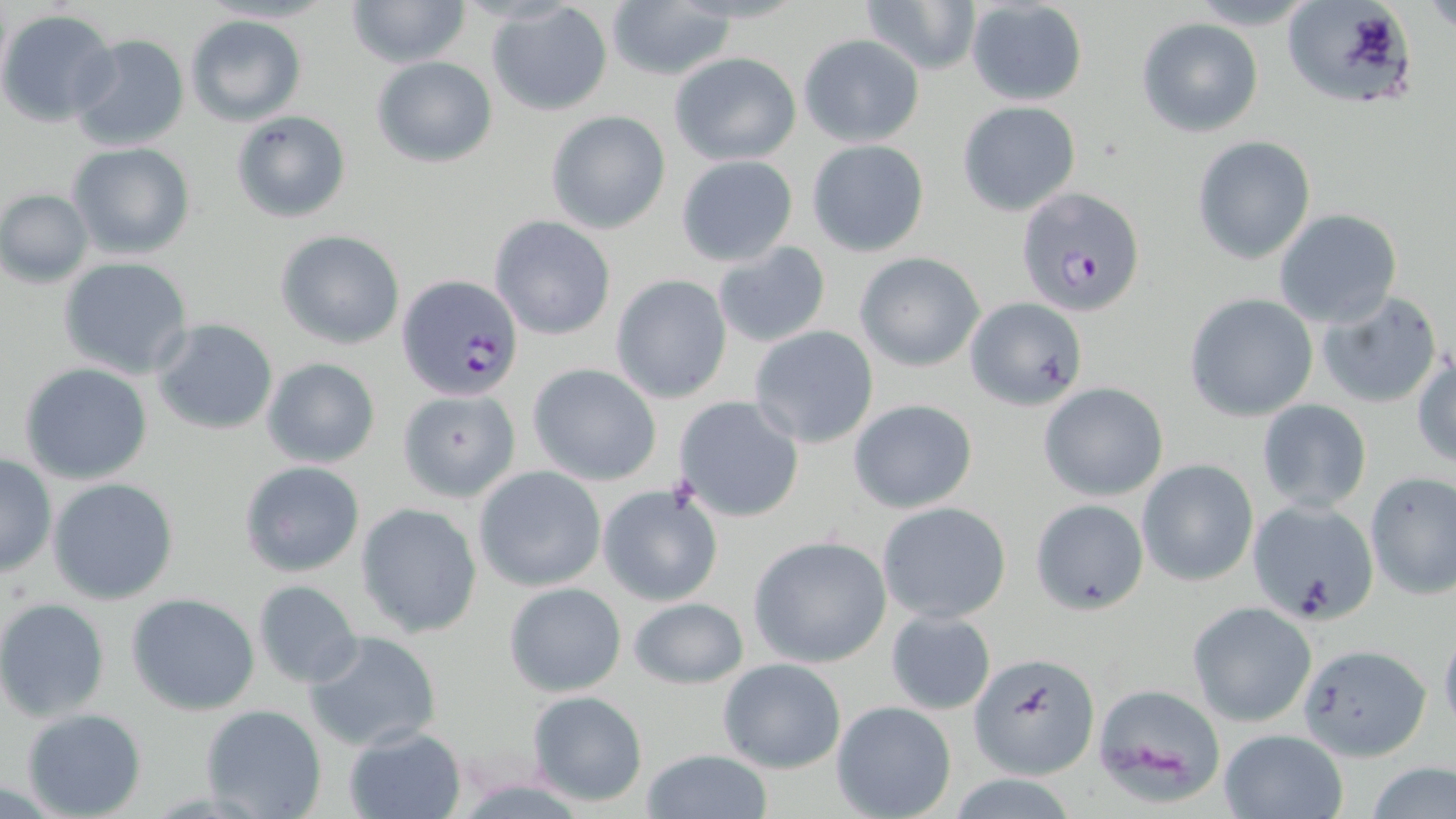

{
  "slide_level_diagnosis": "Plasmodium falciparum",
  "magnification": "1000x",
  "stain": "May-Grünwald-Giemsa",
  "field_of_view": "one of a larger specimen",
  "uninfected_red_blood_cell_locations": "approximate bounding boxes as (x1, y1, x2, y2) in pixels: (346, 0, 470, 68), (860, 0, 981, 77), (1282, 0, 1421, 111), (1424, 0, 1456, 34), (965, 1, 1089, 106), (605, 2, 733, 81), (487, 4, 614, 116), (0, 10, 119, 125), (185, 13, 306, 125), (1135, 16, 1264, 137), (69, 33, 190, 153), (797, 35, 925, 148), (669, 52, 801, 166), (370, 56, 497, 168), (957, 100, 1081, 217), (230, 109, 352, 223), (545, 110, 670, 234), (1192, 135, 1315, 265), (806, 138, 931, 258), (67, 143, 196, 261), (675, 154, 799, 267), (1, 188, 94, 287), (1274, 208, 1403, 328), (489, 216, 615, 341), (276, 230, 405, 349), (712, 240, 833, 350), (854, 251, 984, 371), (59, 257, 194, 379), (611, 274, 733, 403), (1314, 290, 1443, 409), (1185, 293, 1318, 422), (962, 297, 1088, 411), (151, 319, 279, 436), (749, 325, 879, 449), (1412, 355, 1456, 470), (261, 357, 381, 469), (20, 363, 154, 484), (527, 363, 662, 486), (1038, 383, 1168, 501), (398, 388, 520, 502), (673, 395, 805, 522), (848, 399, 979, 514), (1257, 400, 1372, 515), (0, 452, 56, 578), (1137, 458, 1259, 587), (238, 460, 365, 577), (473, 467, 606, 592), (1364, 471, 1455, 600), (47, 478, 179, 604), (598, 484, 722, 607), (1030, 498, 1149, 614), (1246, 499, 1378, 624), (878, 501, 1012, 624), (357, 503, 483, 639), (749, 534, 894, 669), (251, 579, 363, 687), (504, 583, 627, 695), (127, 593, 261, 716), (626, 597, 750, 689), (0, 599, 112, 721), (1189, 602, 1316, 727), (885, 610, 999, 716), (1437, 622, 1456, 740), (302, 629, 443, 753), (1298, 641, 1436, 760), (970, 650, 1098, 780), (718, 657, 847, 775), (1091, 682, 1229, 807), (525, 690, 649, 807), (831, 700, 956, 819), (200, 704, 328, 818), (21, 708, 147, 819), (343, 726, 467, 819), (1217, 728, 1348, 819), (642, 748, 772, 819), (1364, 761, 1455, 819)",
  "modality": "optical microscopy",
  "preparation": "thin blood smear",
  "plasmodium_falciparum_infected_red_blood_cell_locations": "approximate bounding boxes as (x1, y1, x2, y2) in pixels: (1013, 184, 1144, 317), (397, 275, 525, 400)",
  "image_size": "1456×819 pixels"
}